Name the parasite shown.
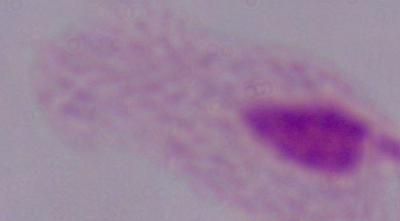
A trichomonad.

Photomicrograph. 1000x magnification.